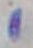
Toxoplasma gondii is seen. Micrograph. Captured at 1000x magnification.